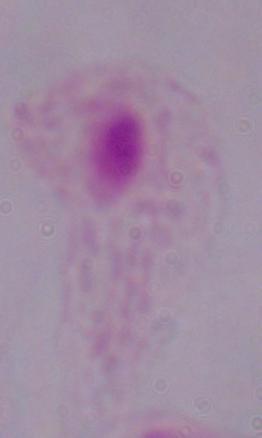
Photomicrograph. A trichomonad is seen. 1000x magnification.